Give the position of every Plasmodium parasite.
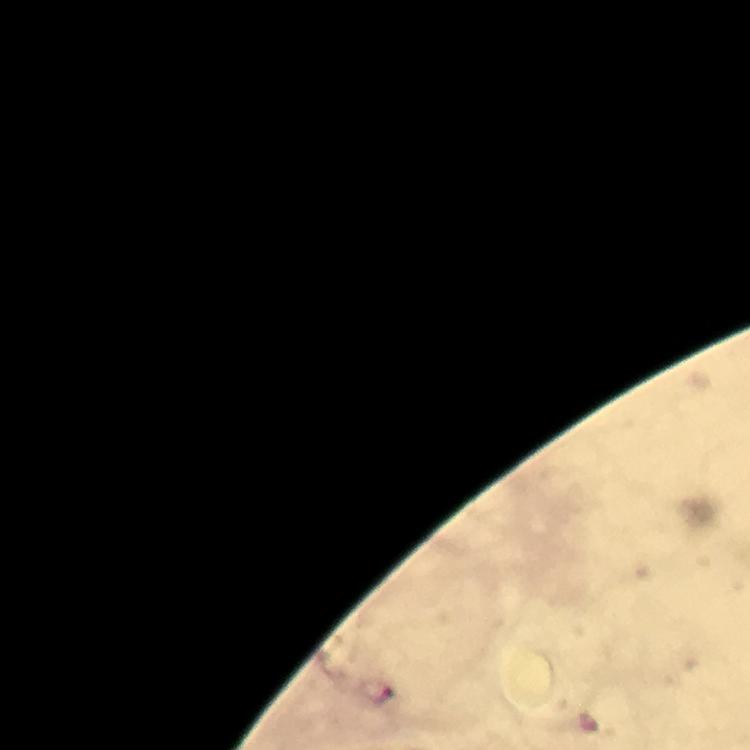

Approximate centers as {x, y} in pixels.
Plasmodium parasites: {377, 694}.

Thick blood smear. Photographed with a smartphone mounted on the microscope. Giemsa-stained preparation. From a malaria diagnostic workup. Image is 750×750 pixels. Cropped region of a single field of view. At 100x magnification. Immersion oil applied.